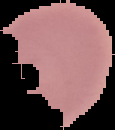

result = negative for Plasmodium parasites
image size = 115×130 pixels
image type = segmented cell region with the area outside set to black
preparation = thin blood film